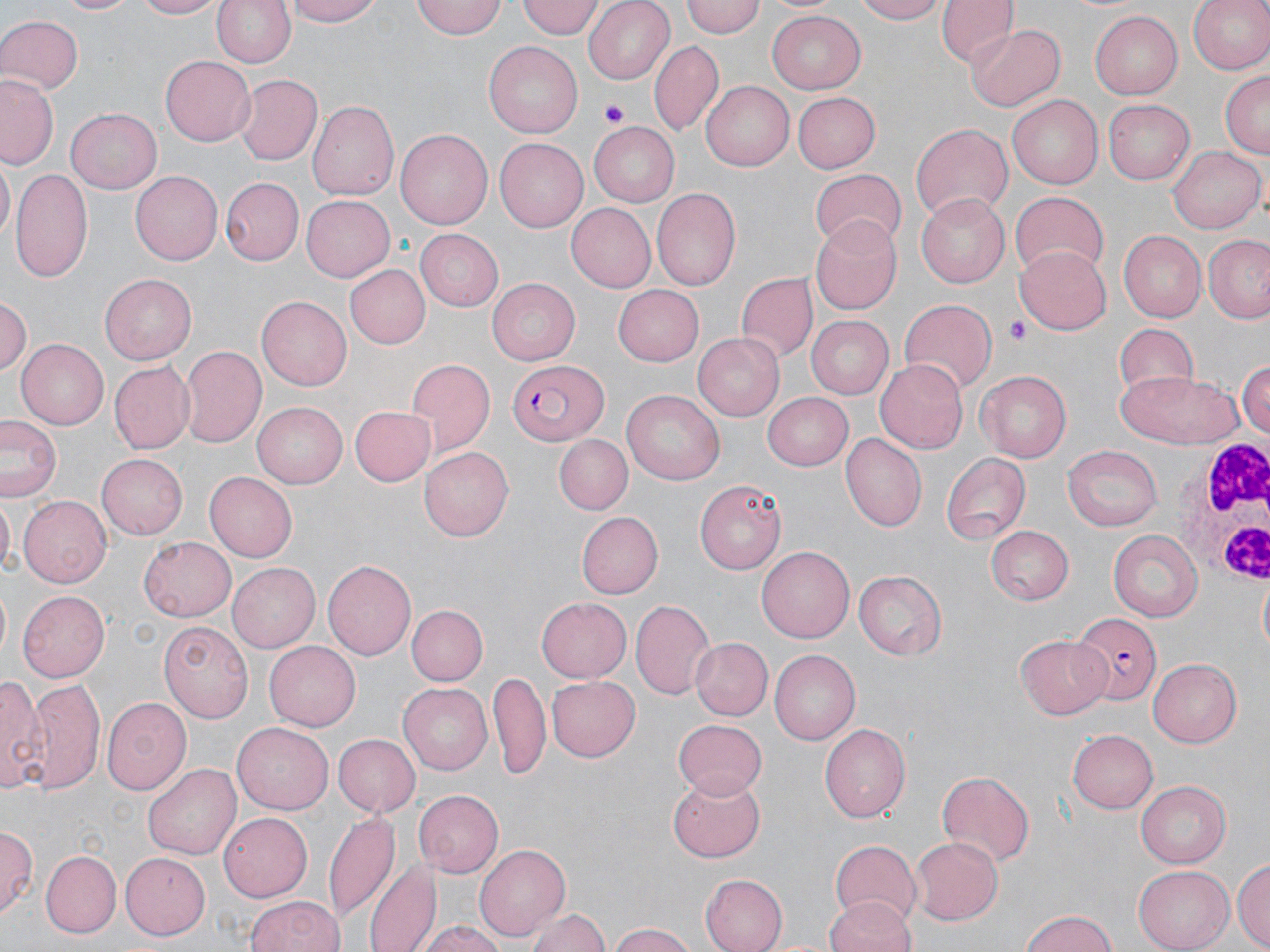
Summary:
  - Coordinate format: approximate bounding boxes as (x1, y1, x2, y2) in pixels
  - Plasmodium falciparum-infected red blood cell locations: (509, 358, 611, 446), (1073, 614, 1161, 704)
  - Platelet locations: (603, 101, 631, 127), (1005, 317, 1029, 346)
  - Uninfected red blood cell locations: (54, 0, 141, 16), (135, 0, 224, 19), (209, 0, 296, 69), (286, 0, 381, 27), (413, 0, 506, 40), (518, 0, 604, 40), (582, 0, 676, 83), (681, 0, 764, 39), (853, 0, 946, 24), (936, 0, 1014, 67), (1186, 0, 1270, 76), (768, 9, 865, 92), (1088, 10, 1182, 99), (0, 16, 81, 95), (967, 24, 1066, 111), (651, 41, 723, 138), (484, 43, 582, 139), (161, 58, 255, 145), (1219, 69, 1269, 161), (0, 73, 60, 169), (234, 74, 323, 165), (702, 81, 795, 171), (1007, 92, 1102, 187), (792, 93, 880, 173), (1104, 97, 1195, 182), (307, 99, 399, 202), (68, 107, 162, 193), (591, 120, 683, 207), (909, 121, 1013, 224), (397, 129, 496, 229), (496, 137, 593, 232), (1167, 145, 1262, 233), (0, 160, 14, 244), (11, 169, 93, 280), (810, 169, 908, 250), (132, 170, 224, 265), (219, 177, 302, 266), (651, 188, 742, 291), (1010, 192, 1109, 279), (917, 193, 1010, 288), (301, 196, 394, 281), (565, 203, 655, 292), (810, 215, 906, 315), (416, 229, 503, 310), (1119, 232, 1205, 323), (1205, 235, 1270, 323), (1017, 243, 1114, 333), (345, 263, 430, 348), (736, 272, 816, 364), (100, 274, 197, 364), (487, 279, 581, 364), (612, 284, 704, 365), (0, 295, 30, 374), (257, 296, 350, 391), (897, 299, 996, 393), (805, 316, 894, 399), (1111, 322, 1201, 399), (692, 332, 782, 421), (16, 338, 111, 429), (180, 344, 266, 446), (1236, 357, 1270, 444), (876, 358, 972, 453), (406, 360, 494, 455), (108, 361, 195, 454), (974, 368, 1072, 463), (1118, 370, 1243, 449), (763, 390, 855, 471), (622, 391, 724, 484), (253, 402, 347, 489), (348, 405, 432, 487), (1, 417, 63, 501), (553, 433, 633, 513), (838, 434, 927, 532), (420, 445, 513, 538), (1062, 446, 1163, 532), (98, 452, 186, 539), (942, 453, 1029, 544), (202, 470, 297, 563), (694, 478, 784, 575), (1, 495, 14, 580), (19, 497, 113, 586), (577, 512, 662, 597), (983, 525, 1072, 606), (1107, 531, 1202, 623), (137, 535, 236, 623), (757, 546, 853, 643), (324, 559, 416, 661), (228, 563, 321, 653), (853, 571, 945, 660), (17, 591, 111, 680), (536, 597, 630, 683), (630, 598, 716, 700), (409, 605, 488, 686), (162, 619, 254, 722), (1017, 632, 1115, 717), (691, 638, 774, 720), (263, 641, 360, 730), (769, 648, 861, 742), (1149, 660, 1243, 746), (489, 671, 551, 784), (0, 674, 48, 795), (548, 675, 640, 762), (22, 678, 106, 793), (398, 681, 493, 774), (102, 696, 193, 796), (673, 717, 767, 800), (233, 722, 334, 813), (819, 722, 910, 824), (1070, 729, 1161, 814), (331, 733, 418, 814), (143, 762, 241, 862), (935, 771, 1036, 867), (668, 773, 766, 863), (1135, 779, 1232, 868), (413, 788, 503, 876), (325, 809, 401, 925), (218, 813, 312, 903), (0, 824, 37, 919), (911, 836, 1002, 923), (830, 838, 923, 927), (474, 843, 568, 939), (42, 852, 120, 936), (121, 853, 210, 937), (1232, 859, 1270, 949), (368, 860, 441, 952), (1135, 866, 1233, 951), (699, 874, 786, 952), (244, 895, 346, 952), (825, 895, 916, 952), (527, 905, 610, 952), (1020, 909, 1118, 952), (419, 921, 506, 952), (609, 923, 699, 952)
  - White blood cell locations: (1171, 438, 1270, 582)
  - Slide-level diagnosis: Plasmodium falciparum
  - Stain: May-Grünwald-Giemsa
  - Image size: 1270×952 pixels
  - Preparation: thin blood film
  - Modality: light microscopy
  - Magnification: 1000x
  - Field of view: one of a larger specimen